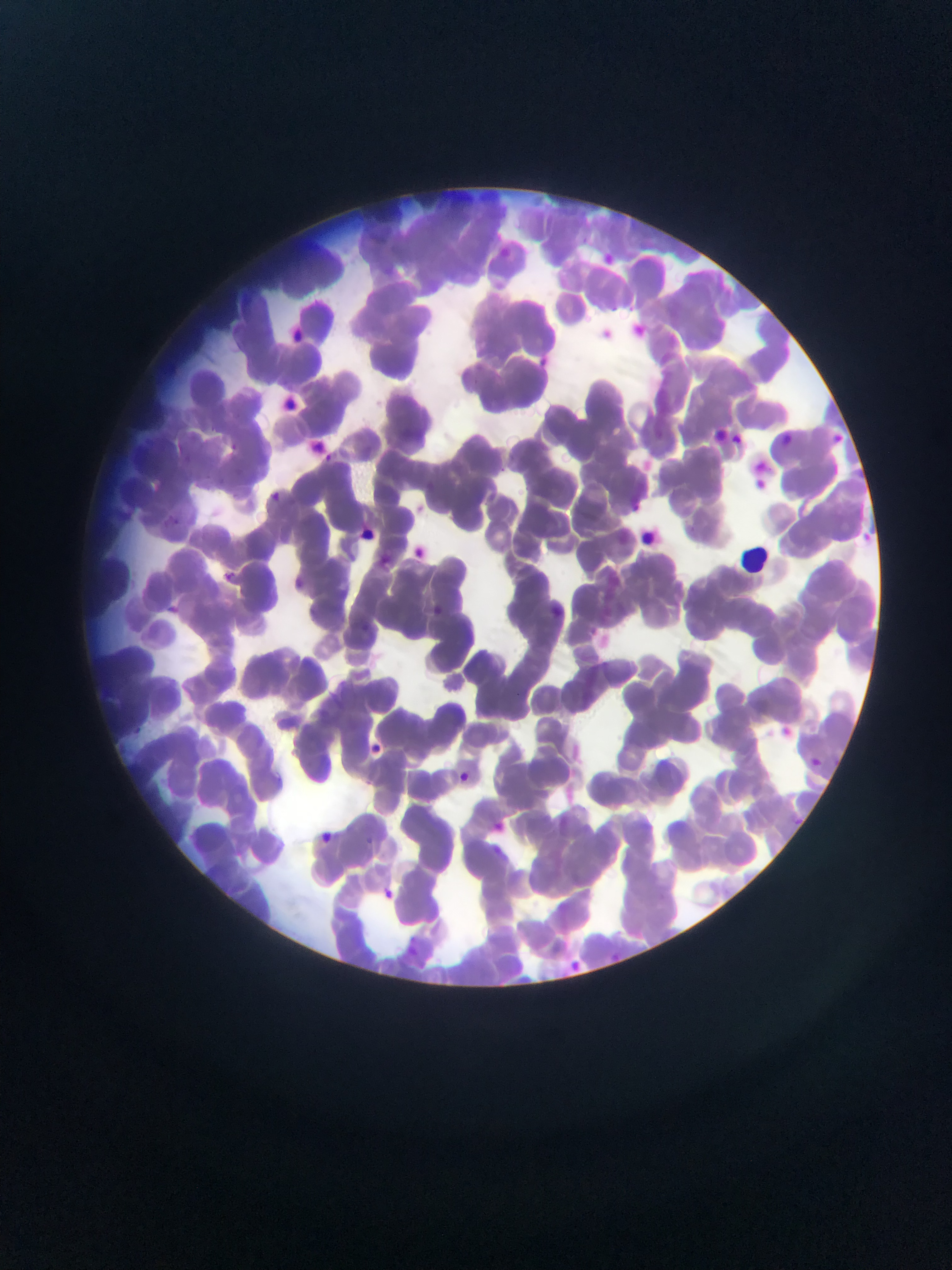

Approximate bounding boxes as {left, top, right, bottom} in pixels. Malaria parasite locations: {595, 251, 613, 270}, {609, 300, 618, 317}, {625, 303, 635, 311}, {636, 322, 653, 336}, {534, 355, 553, 367}, {732, 429, 746, 450}, {832, 429, 849, 447}, {780, 431, 804, 448}, {224, 440, 240, 452}, {314, 450, 335, 467}, {756, 459, 765, 472}, {756, 478, 768, 491}, {267, 489, 281, 503}, {859, 526, 874, 545}, {412, 542, 430, 560}, {216, 569, 241, 586}, {164, 601, 189, 618}, {433, 603, 453, 626}, {772, 720, 793, 740}, {368, 738, 389, 766}, {807, 753, 824, 773}, {455, 767, 477, 790}, {490, 815, 509, 836}, {314, 830, 337, 849}, {378, 875, 392, 898}, {604, 949, 622, 963}, {572, 955, 591, 975}. Image is 952×1270 pixels. Sample from Ghana. Photographed through a microscope with a mobile-phone camera. Thin blood film. One field of view.